Report the malaria status of this cell.
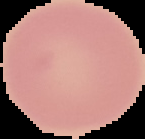
It is uninfected.

Summary:
  - Image type: segmented cell region on a black background
  - Image size: 145×139 pixels
  - Preparation: thin blood film